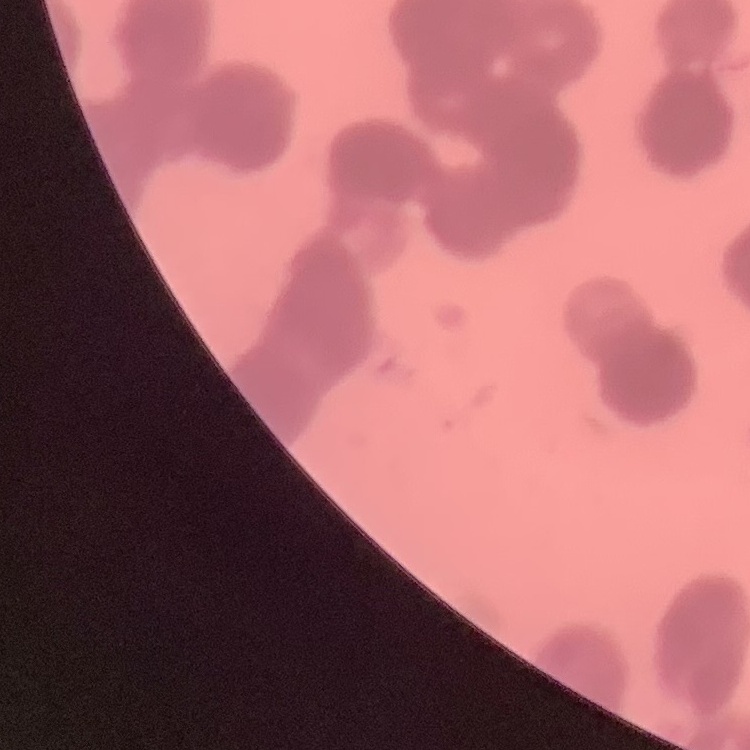

Summary:
  - Erythrocyte morphology: rouleaux formation
  - Image type: one tile cut from a larger photomicrograph
  - Stain: Field's or Giemsa
  - Preparation: thin blood film